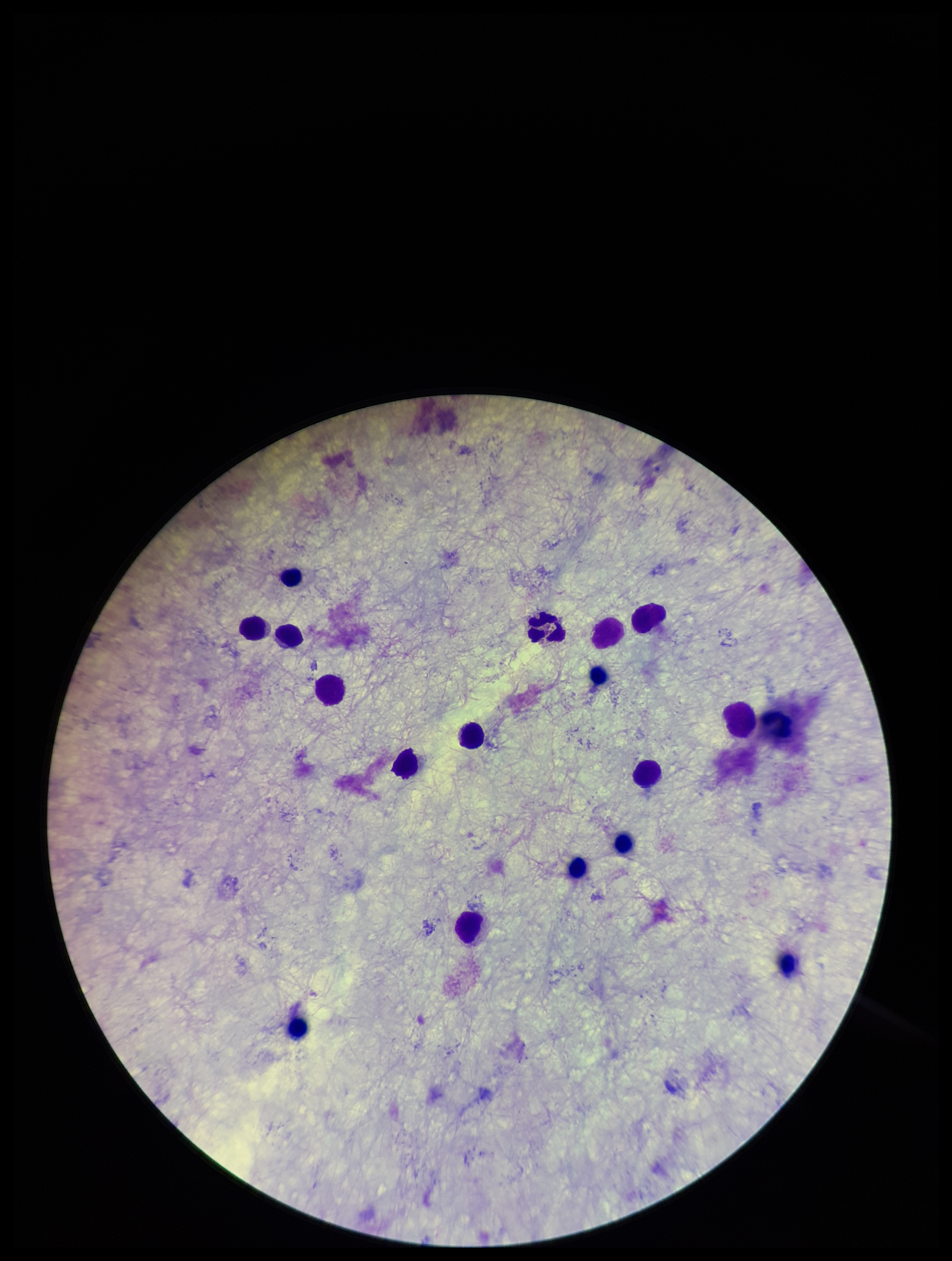 Leukocyte count: 15. Plasmodium parasites: none seen. Patient malaria status: negative. Preparation: thick. Giemsa stain. One field from this slide. Parasite count: 0. Image is 952×1261 pixels. Photographed through the microscope eyepiece with a smartphone camera.